Evaluate for parasitized red blood cells.
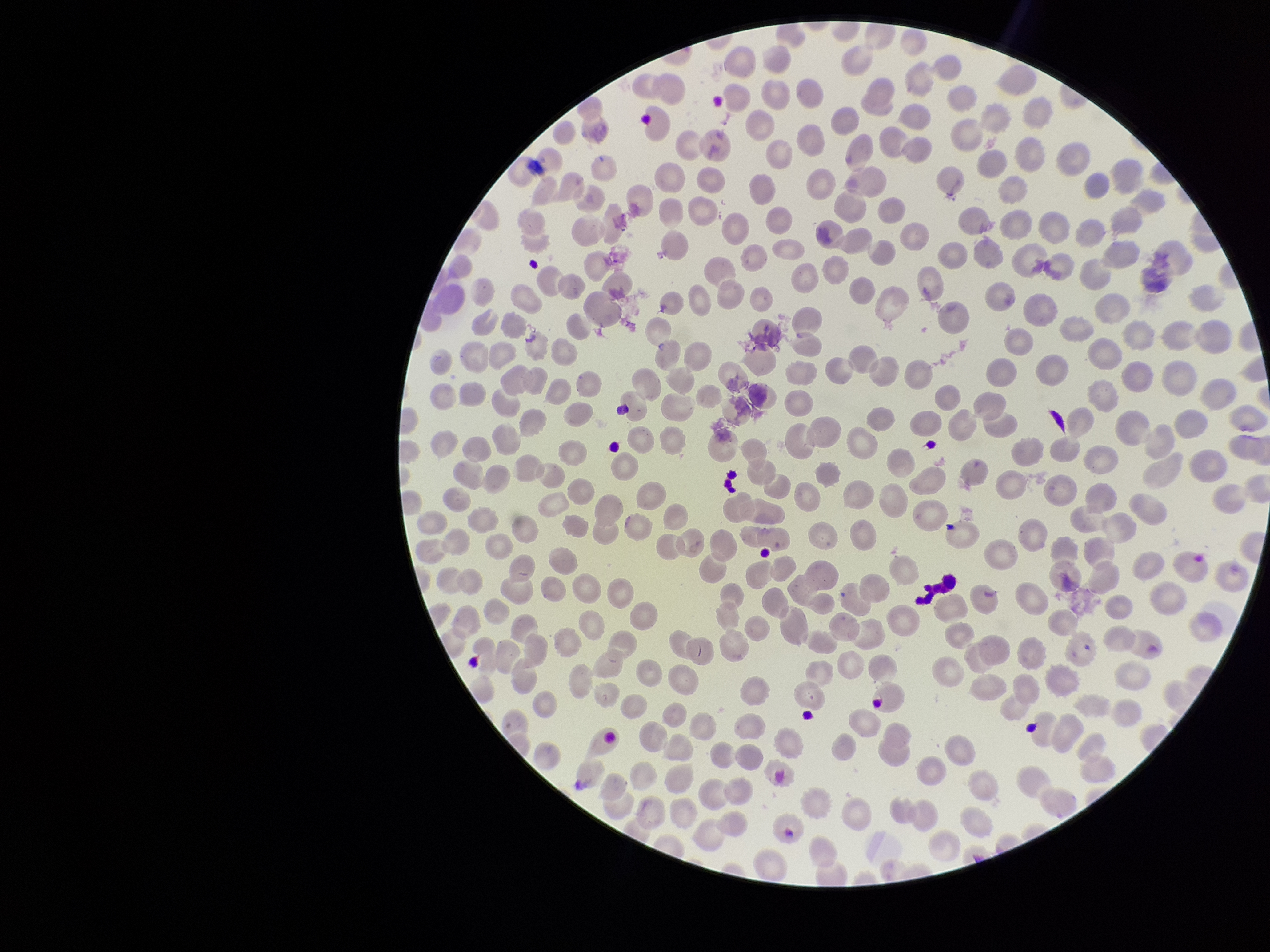

None seen.

Summary:
  - Capture: smartphone photograph through the microscope eyepiece
  - Species reported for this patient: Plasmodium falciparum
  - Image size: 1270×952 pixels
  - Patient malaria status: infected
  - Red blood cell count: 245
  - Preparation: thin blood smear
  - Field of view: one from this slide
  - Parasitized red blood cell count: 0
  - Stain: Giemsa